Locate every blood parasite and identify its species.
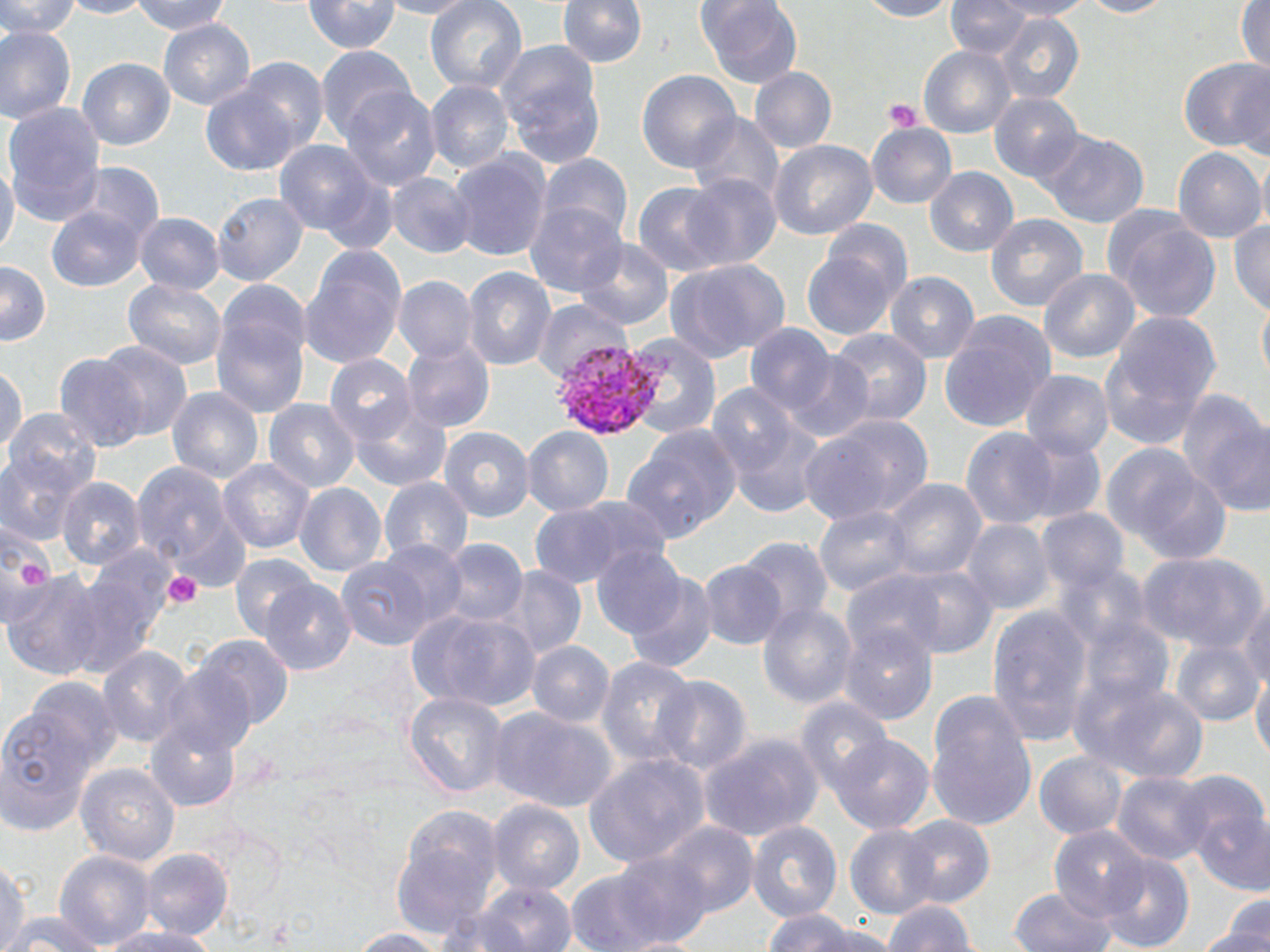

Approximate bounding boxes as (x1, y1, x2, y2) in pixels.
Plasmodium vivax-infected red blood cells: (549, 336, 665, 444).
No Plasmodium falciparum, Plasmodium ovale, Plasmodium malariae, Babesia divergens, or Trypanosoma brucei observed.

Summary:
  - Uninfected red blood cell locations: (1, 0, 80, 38), (55, 0, 150, 19), (130, 0, 234, 35), (374, 0, 476, 20), (425, 0, 527, 93), (859, 0, 957, 21), (945, 0, 1030, 59), (990, 0, 1093, 21), (1080, 0, 1172, 18), (558, 1, 646, 69), (697, 1, 801, 88), (305, 2, 400, 54), (1236, 2, 1269, 75), (996, 13, 1085, 105), (158, 19, 255, 109), (0, 26, 76, 125), (315, 45, 415, 139), (494, 45, 605, 163), (918, 45, 1014, 138), (234, 56, 328, 151), (1179, 56, 1270, 153), (77, 58, 174, 150), (1231, 62, 1268, 162), (749, 67, 836, 152), (637, 69, 740, 173), (425, 80, 515, 173), (201, 85, 302, 177), (339, 87, 441, 190), (989, 93, 1083, 183), (2, 102, 107, 223), (688, 113, 784, 206), (867, 122, 957, 208), (1040, 129, 1149, 229), (272, 139, 380, 238), (767, 140, 877, 240), (1256, 146, 1270, 240), (1172, 147, 1266, 241), (447, 150, 554, 263), (537, 153, 631, 245), (0, 158, 20, 258), (74, 162, 164, 246), (925, 165, 1018, 257), (386, 172, 477, 259), (684, 173, 782, 269), (633, 182, 730, 274), (212, 193, 309, 285), (526, 201, 628, 297), (47, 206, 148, 293), (133, 212, 225, 295), (986, 213, 1089, 312), (1107, 215, 1220, 324), (819, 218, 913, 303), (1229, 219, 1270, 316), (574, 238, 675, 331), (300, 248, 406, 368), (801, 248, 899, 340), (667, 259, 790, 362), (1, 261, 51, 346), (462, 266, 556, 370), (1038, 268, 1140, 362), (885, 272, 980, 362), (392, 275, 480, 363), (216, 278, 311, 362), (123, 279, 228, 370), (1256, 290, 1270, 388), (532, 297, 631, 384), (1105, 310, 1223, 422), (938, 314, 1056, 434), (211, 315, 308, 417), (745, 323, 836, 413), (825, 328, 932, 427), (623, 334, 721, 438), (402, 339, 494, 433), (97, 341, 191, 441), (780, 352, 874, 442), (55, 353, 146, 451), (324, 355, 418, 446), (0, 362, 26, 453), (1019, 369, 1114, 458), (707, 384, 802, 477), (167, 385, 263, 484), (1179, 391, 1269, 513), (263, 399, 361, 492), (350, 404, 451, 491), (2, 407, 101, 498), (798, 413, 934, 526), (726, 416, 827, 520), (625, 424, 742, 540), (438, 425, 535, 520), (522, 426, 614, 516), (960, 427, 1062, 530), (1013, 431, 1106, 523), (906, 440, 1029, 568), (1103, 444, 1228, 560), (0, 455, 83, 544), (218, 460, 315, 552), (132, 462, 242, 570), (57, 477, 146, 569), (380, 477, 473, 564), (883, 479, 988, 579), (294, 483, 387, 576), (527, 499, 664, 587), (814, 506, 914, 596), (1035, 508, 1130, 592), (960, 518, 1056, 615), (0, 525, 55, 624), (738, 536, 834, 633), (439, 538, 527, 626), (374, 541, 468, 630), (590, 545, 688, 639), (1135, 550, 1268, 653), (69, 552, 174, 671), (230, 552, 319, 643), (336, 554, 438, 650), (698, 560, 789, 649), (1054, 563, 1153, 652), (893, 564, 1000, 658), (501, 565, 586, 660), (4, 570, 107, 681), (838, 570, 950, 666), (622, 572, 717, 672), (260, 577, 357, 675), (1237, 597, 1270, 691), (757, 603, 857, 708), (986, 605, 1095, 742), (412, 609, 541, 712), (1078, 617, 1176, 708), (836, 622, 939, 725), (192, 635, 294, 729), (1171, 640, 1264, 725), (526, 641, 615, 725), (97, 645, 193, 747), (596, 656, 699, 765), (160, 663, 259, 757), (1250, 668, 1270, 765), (652, 675, 755, 774), (22, 676, 122, 770), (1076, 677, 1207, 782), (404, 690, 510, 798), (927, 696, 1037, 828), (794, 697, 895, 793), (487, 705, 618, 813), (0, 711, 96, 834), (145, 718, 241, 811), (698, 730, 826, 842), (830, 733, 936, 835), (1033, 751, 1127, 840), (585, 754, 710, 865), (75, 762, 181, 865), (1111, 770, 1213, 864), (1172, 770, 1268, 851), (488, 800, 584, 895), (1193, 807, 1270, 896), (394, 812, 501, 931), (897, 815, 995, 908), (656, 820, 759, 917), (747, 820, 842, 921), (844, 824, 944, 918), (1049, 826, 1150, 921), (140, 847, 233, 940), (54, 849, 158, 949), (607, 850, 717, 948), (1099, 851, 1194, 951), (0, 861, 31, 949), (565, 867, 671, 951), (476, 881, 576, 952), (1010, 888, 1115, 952), (882, 900, 978, 952), (1209, 906, 1270, 951), (437, 909, 534, 951), (762, 910, 860, 952), (4, 911, 101, 952), (798, 924, 905, 952), (104, 925, 219, 952), (1197, 927, 1270, 952), (349, 928, 445, 951), (597, 936, 721, 951)
  - Platelet locations: (883, 99, 923, 133), (162, 571, 201, 610)
  - Slide-level diagnosis: Plasmodium vivax
  - Modality: optical microscopy
  - Preparation: thin blood film
  - Stain: May-Grünwald-Giemsa
  - Field of view: one of a larger specimen
  - Image size: 1270×952 pixels
  - Magnification: 1000x